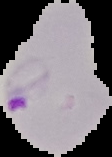
preparation: thin blood film
image_type: segmented cell region with the area outside set to black
malaria_status: parasitized
image_size: 112×157 pixels